State the preparation type.
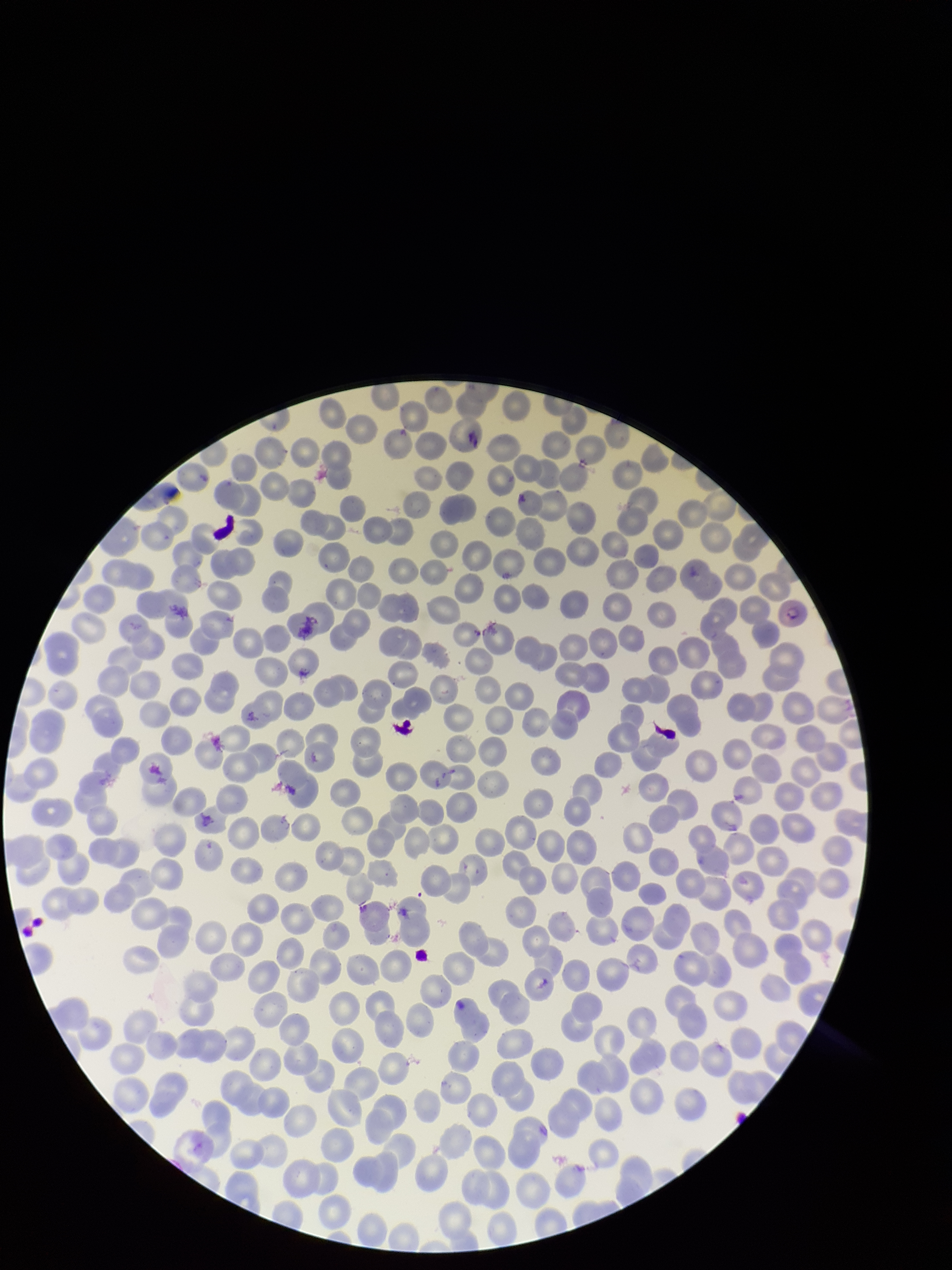

It is a thin blood smear.

patient malaria status = positive
capture = smartphone photograph through the microscope eyepiece
parasitized red blood cells = identified
image size = 952×1270 pixels
parasitized red blood cell count = 1
species reported for this patient = Plasmodium vivax
stain = Giemsa
field of view = single
red blood cell count = 303